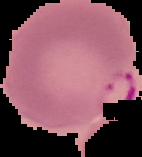
image type = cell region segmented out of the field of view; surrounding area masked to black
preparation = thin blood smear
image size = 142×157 pixels
malaria status = parasitized